Describe the morphology of the erythrocytes.
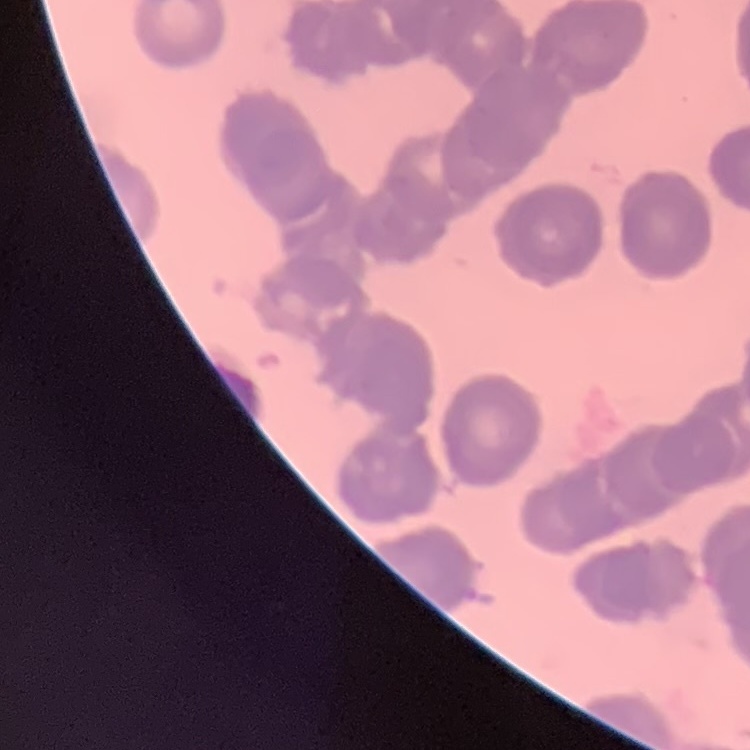
They show rouleaux formation.

image type = square crop of a larger photomicrograph
preparation = thin peripheral smear
stain = Field's or Giemsa